Identify the parasite.
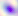

This is Toxoplasma gondii.

Summary:
  - Magnification: 400x
  - Modality: micrograph